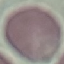

malaria status = uninfected
image type = automatically extracted cell patch, resized to 64 × 64 pixels
preparation = thin smear
capture = smartphone camera at the microscope eyepiece
stain = Giemsa